Assess the morphology of the erythrocytes.
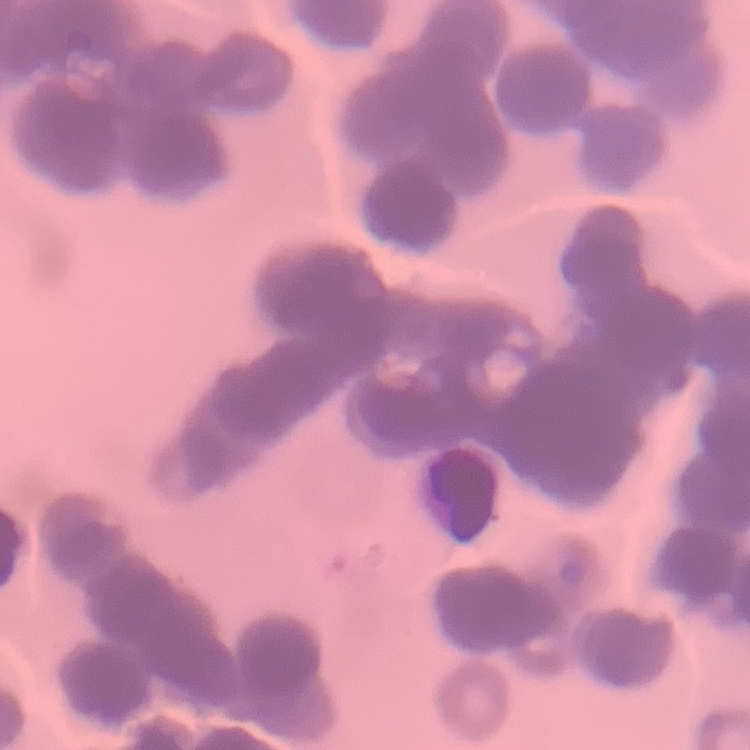

They show rouleaux formation.

preparation = thin blood smear
image type = square crop of a larger photomicrograph
stain = Field's or Giemsa